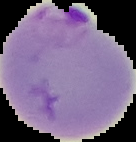

{
  "image_type": "segmented cell region with the area outside set to black",
  "result": "Plasmodium parasites identified",
  "preparation": "thin blood film",
  "image_size": "136×142 pixels"
}